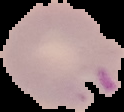 The area outside the segmented cell region is set to black. Result: Plasmodium parasites identified. Image is 124×112 pixels. From a thin blood film.